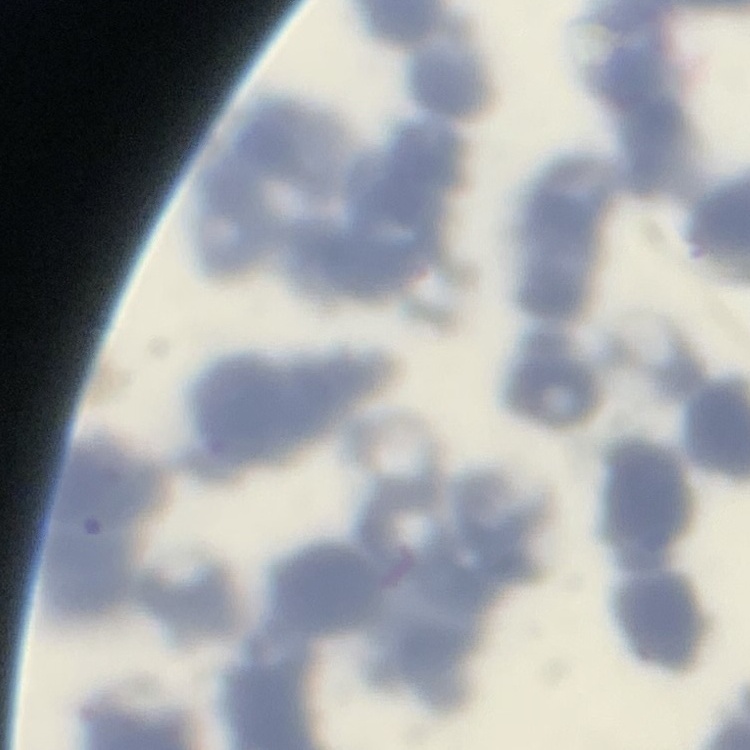

The erythrocytes exhibit rouleaux formation. One tile cut from a larger photomicrograph. Stained with either Field's or Giemsa. Thin blood smear.